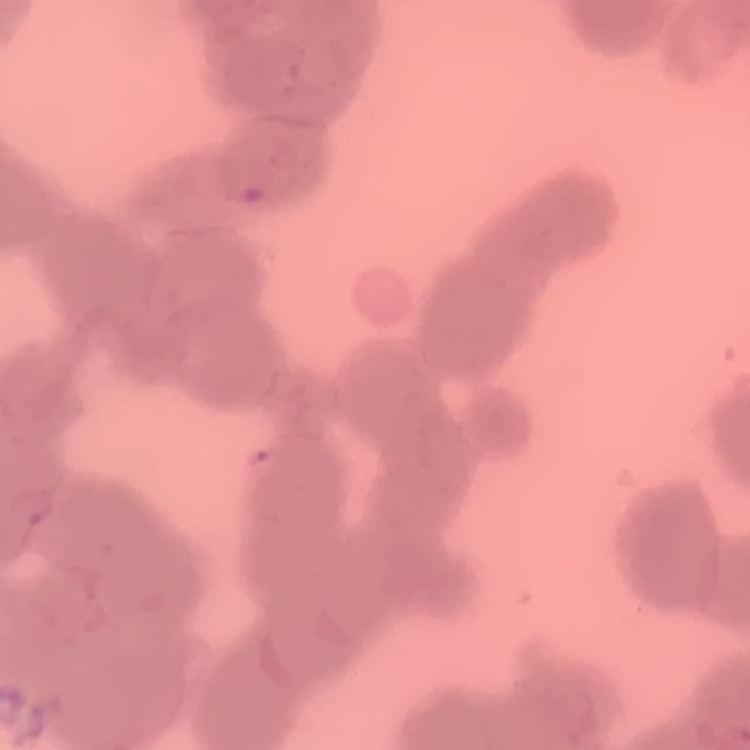
red blood cell morphology = rouleaux formation
stain = Field's or Giemsa
image type = one tile cut from a larger photomicrograph
preparation = thin peripheral smear